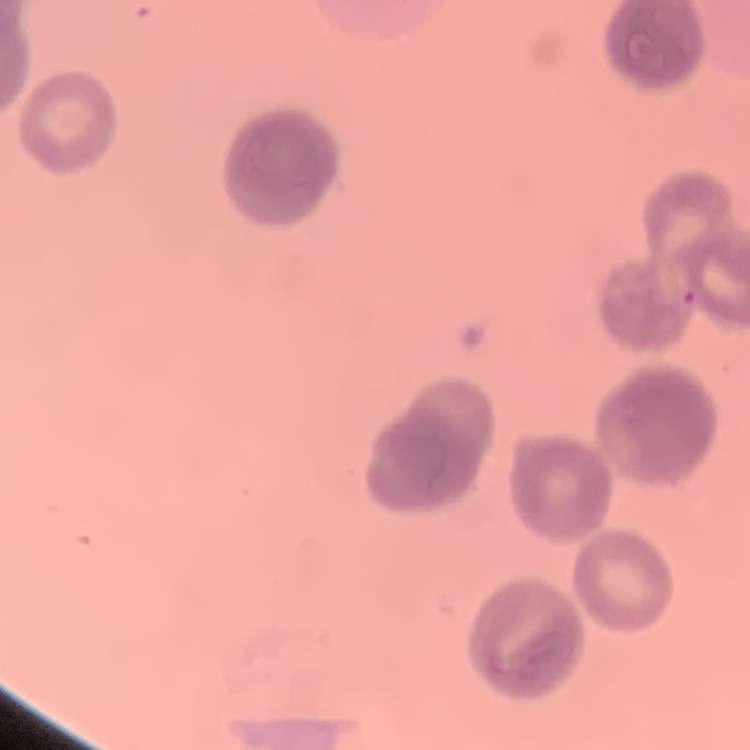
{
  "red_blood_cell_morphology": "rouleaux formation",
  "stain": "Field's or Giemsa",
  "preparation": "thin peripheral smear",
  "image_type": "square crop of a larger photomicrograph"
}